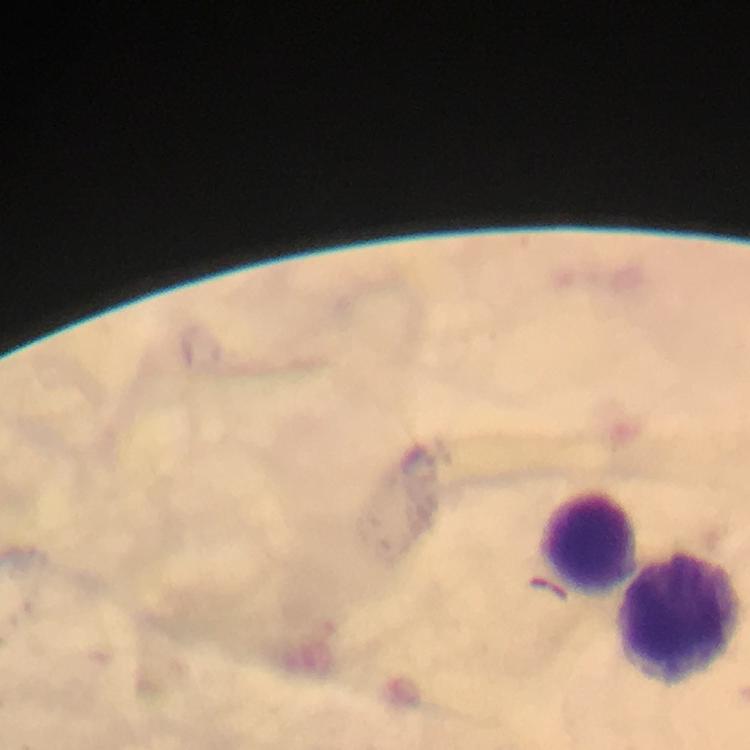

Approximate centers as (x, y) in pixels.
Summary:
  - Leukocyte locations: (587, 542), (677, 617)
  - Plasmodium parasites: none seen
  - Stain: Giemsa
  - Image size: 750×750 pixels
  - Immersion oil: used
  - Cropped from: a single field of view
  - Preparation: thick blood film
  - Magnification: 100x
  - Context: from a diagnostic examination for malaria
  - Capture: smartphone photograph through a microscope